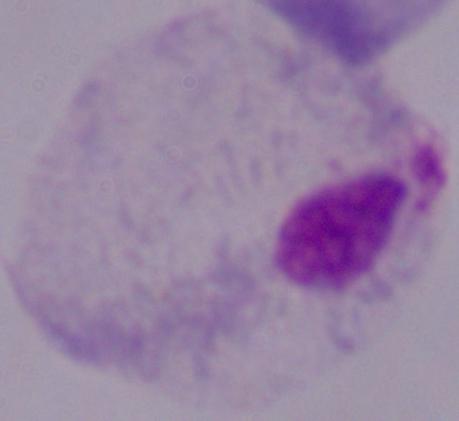

Summary:
  - Modality: micrograph
  - Magnification: 1000x
  - Identification: trichomonad